Give the position of every leukocyte visible.
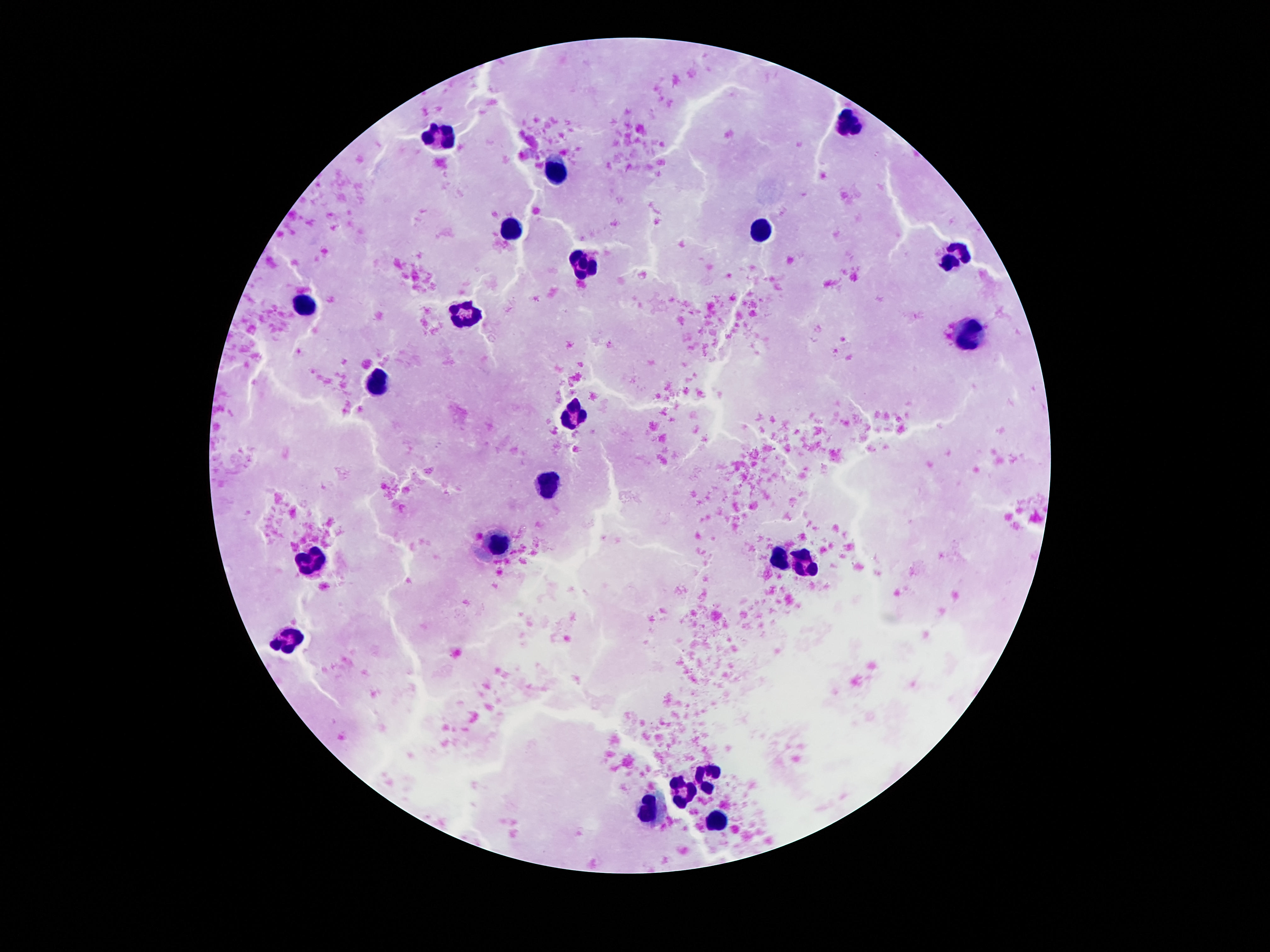

Approximate object centers, in pixels from the top-left corner.
Leukocytes: (x=851, y=120), (x=443, y=136), (x=561, y=172), (x=513, y=232), (x=763, y=234), (x=953, y=256), (x=587, y=260), (x=305, y=306), (x=471, y=313), (x=969, y=336), (x=377, y=384), (x=571, y=414), (x=551, y=486), (x=503, y=542), (x=775, y=557), (x=313, y=563), (x=805, y=563), (x=289, y=637), (x=705, y=773), (x=681, y=796), (x=649, y=812), (x=715, y=823).

Single field of view. Image is 1270×952 pixels. Giemsa stain. 100x magnification. Patient malaria status: uninfected. Smartphone photograph taken through the microscope eyepiece. Thick blood film.